Identify the blood parasite species.
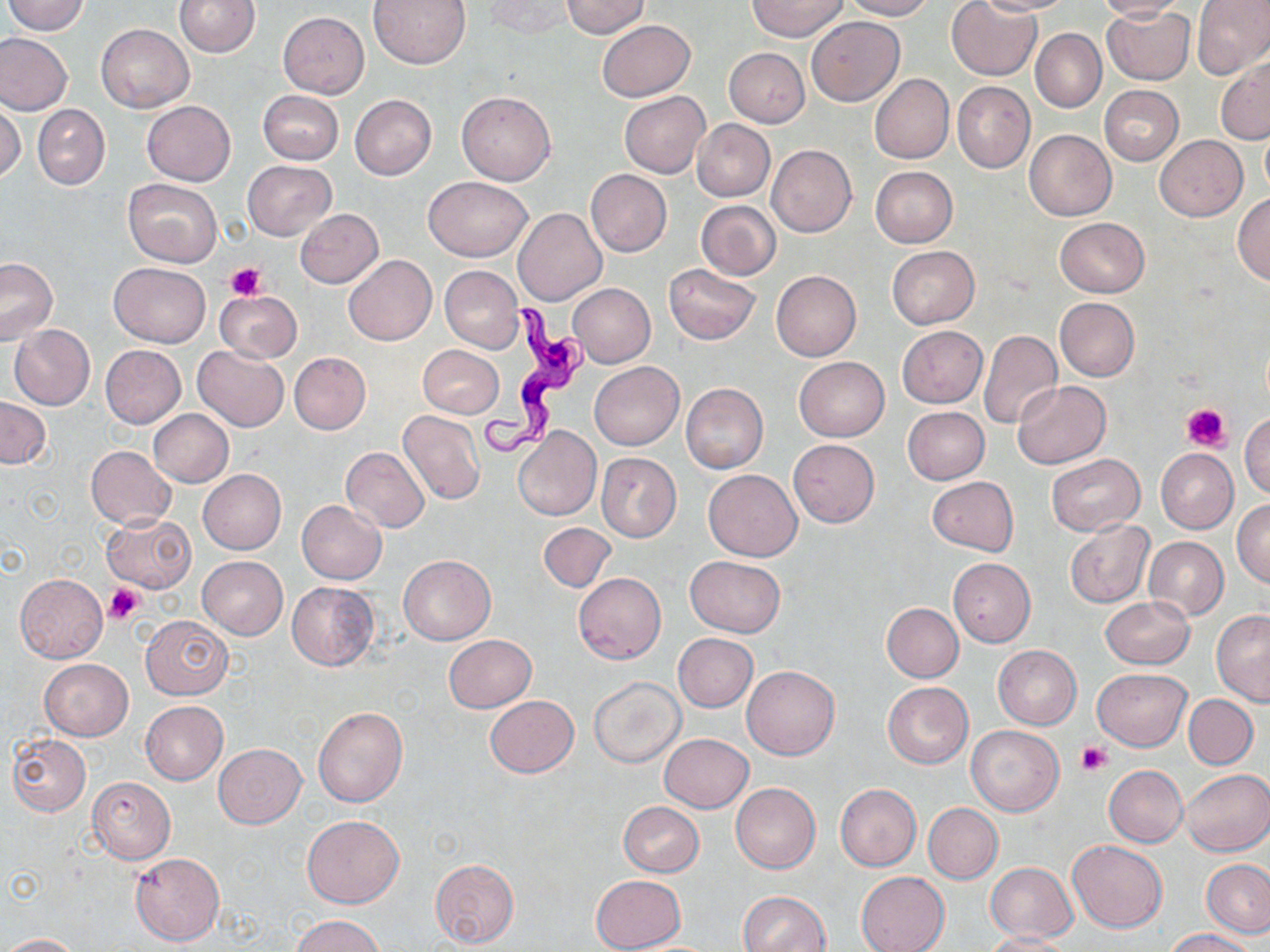
Trypanosoma brucei.

preparation = thin blood film
field of view = one of a larger specimen
uninfected red blood cell locations = approximate bounding boxes as [x1, y1, x2, y2] in pixels: [5, 0, 89, 35], [367, 0, 473, 69], [484, 0, 573, 40], [560, 0, 650, 38], [749, 0, 846, 40], [845, 0, 933, 21], [946, 0, 1041, 81], [976, 0, 1074, 14], [1094, 0, 1187, 21], [1192, 0, 1270, 79], [175, 1, 259, 57], [1103, 5, 1195, 85], [278, 11, 368, 97], [805, 17, 904, 105], [597, 20, 695, 100], [96, 23, 194, 113], [1030, 29, 1106, 112], [0, 32, 73, 117], [724, 47, 810, 127], [1217, 58, 1270, 144], [869, 74, 954, 163], [953, 82, 1035, 173], [1099, 84, 1183, 165], [258, 89, 344, 164], [456, 91, 556, 185], [619, 91, 709, 178], [350, 95, 436, 180], [0, 100, 25, 184], [142, 101, 235, 185], [33, 104, 110, 190], [692, 119, 774, 202], [1261, 125, 1270, 197], [1024, 129, 1117, 220], [691, 130, 849, 214], [1156, 136, 1246, 220], [767, 145, 856, 236], [243, 160, 336, 242], [870, 166, 959, 247], [585, 169, 671, 256], [424, 176, 533, 261], [124, 178, 222, 267], [1233, 193, 1270, 285], [696, 201, 782, 279], [514, 208, 606, 306], [295, 209, 384, 288], [1054, 217, 1150, 298], [887, 245, 979, 328], [344, 255, 437, 345], [0, 258, 58, 345], [109, 262, 210, 348], [663, 264, 761, 344], [440, 266, 523, 352], [771, 270, 861, 360], [568, 283, 655, 367], [215, 290, 301, 363], [1055, 297, 1139, 381], [9, 325, 94, 410], [897, 325, 986, 407], [979, 330, 1061, 429], [100, 344, 186, 428], [418, 344, 504, 417], [192, 345, 290, 431], [289, 353, 371, 434], [794, 357, 888, 441], [590, 362, 683, 450], [1011, 381, 1110, 469], [681, 383, 768, 473], [0, 397, 51, 468], [902, 406, 990, 485], [149, 409, 233, 488], [398, 409, 485, 505], [1239, 412, 1270, 497], [514, 427, 601, 521], [788, 439, 880, 527], [86, 446, 176, 530], [342, 447, 430, 532], [1155, 448, 1238, 534], [596, 453, 681, 541], [1047, 453, 1144, 534], [198, 469, 286, 553], [703, 469, 802, 561], [927, 476, 1018, 554], [1232, 498, 1270, 589], [296, 501, 387, 585], [101, 511, 197, 592], [1064, 519, 1153, 608], [538, 522, 615, 593], [1144, 536, 1228, 620], [399, 555, 496, 644], [198, 556, 287, 639], [684, 556, 786, 638], [947, 558, 1035, 647], [574, 573, 666, 663], [15, 574, 107, 662], [286, 582, 381, 671], [1100, 595, 1193, 669], [882, 603, 964, 682], [1212, 609, 1270, 704], [140, 616, 232, 699], [673, 632, 758, 712], [443, 635, 536, 712], [992, 645, 1081, 729], [38, 659, 133, 741], [742, 665, 839, 759], [1091, 668, 1191, 750], [589, 676, 685, 768], [882, 681, 973, 768], [1184, 694, 1257, 769], [484, 695, 579, 778], [141, 701, 227, 784], [313, 707, 407, 807], [966, 725, 1063, 816], [8, 734, 91, 816], [659, 734, 753, 813], [213, 743, 306, 828], [1104, 765, 1187, 846], [1181, 768, 1270, 856], [87, 777, 175, 863], [731, 782, 820, 873], [835, 783, 921, 871], [618, 801, 704, 877], [924, 803, 1002, 884], [302, 814, 404, 909], [1067, 840, 1167, 932], [131, 853, 224, 946], [430, 859, 519, 946], [1202, 859, 1270, 937], [985, 862, 1077, 942], [856, 871, 949, 952], [590, 875, 686, 952], [738, 891, 831, 952], [290, 914, 386, 952], [1165, 929, 1257, 952], [982, 932, 1071, 952], [2, 933, 79, 951]
magnification = 1000x
stain = May-Grünwald-Giemsa
modality = light microscopy
Trypanosoma brucei locations = approximate bounding boxes as [x1, y1, x2, y2] in pixels: [476, 304, 595, 466]
image size = 1270×952 pixels
platelet locations = approximate bounding boxes as [x1, y1, x2, y2] in pixels: [225, 261, 265, 298], [1181, 401, 1231, 451], [105, 583, 143, 623], [1078, 741, 1111, 774]